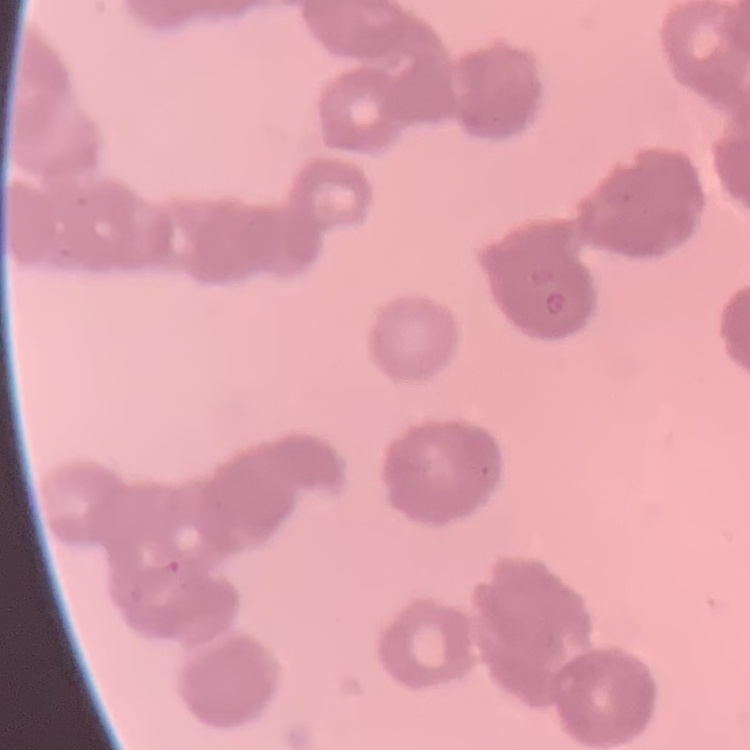

{
  "erythrocyte_morphology": "rouleaux formation",
  "stain": "Field's or Giemsa",
  "image_type": "square crop of a larger photomicrograph",
  "preparation": "thin blood film"
}